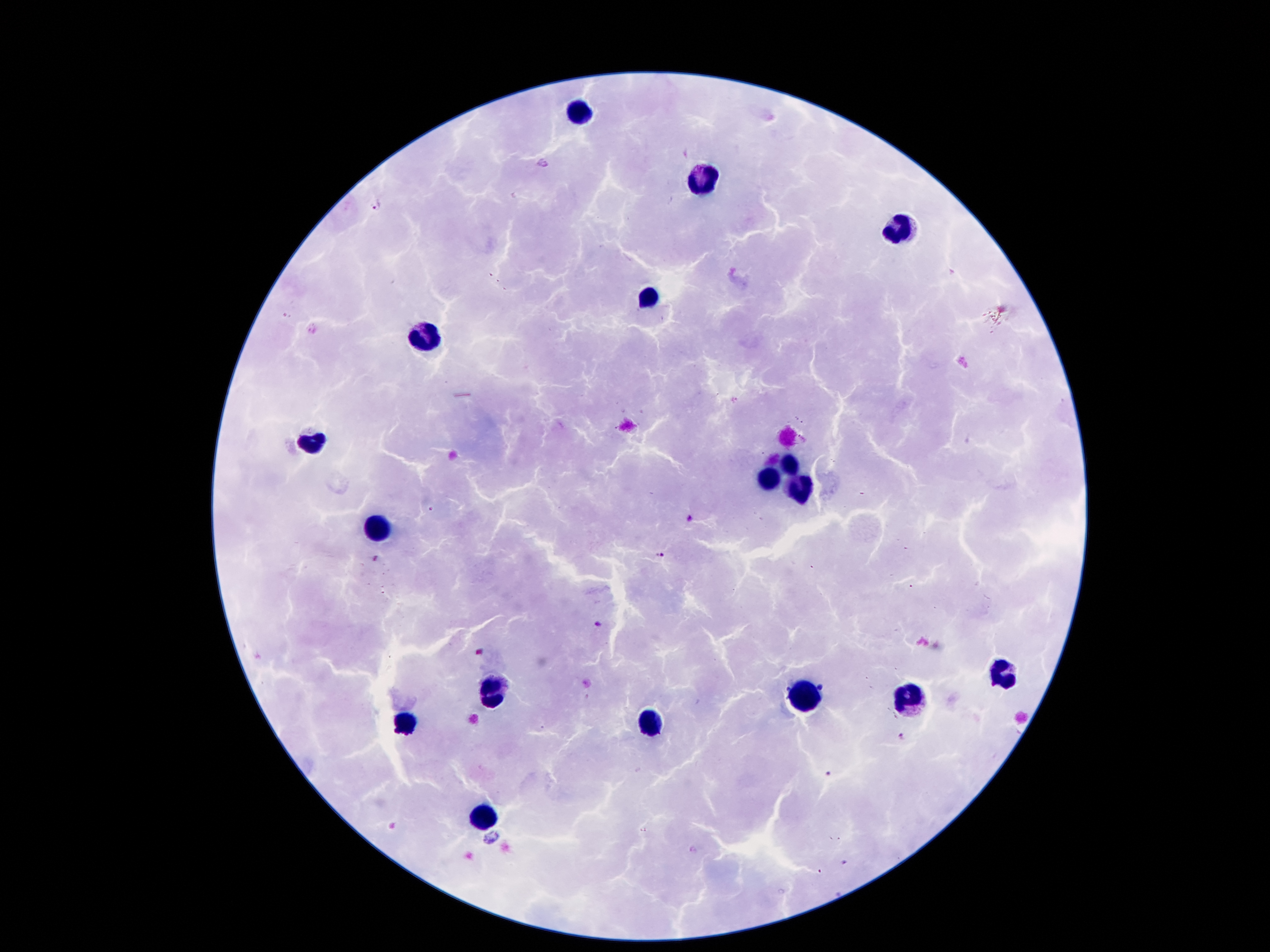

coordinate format = approximate centers as [x, y] in pixels
malaria parasite locations = [377, 206], [687, 518], [660, 555], [599, 624], [904, 738], [826, 774], [491, 836], [845, 862]
leukocyte locations = [578, 113], [699, 178], [899, 229], [645, 300], [424, 336], [311, 441], [788, 466], [767, 481], [798, 487], [380, 525], [1000, 674], [496, 693], [800, 697], [911, 697], [649, 722], [407, 724], [485, 816]
preparation = thick blood film
capture = smartphone camera through the microscope eyepiece
stain = Giemsa
patient malaria status = infected with Plasmodium falciparum
field of view = one from this slide
image size = 1270×952 pixels
magnification = 100x